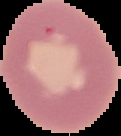
From a thin blood smear. The area outside the segmented cell region is set to black. Result: no malaria parasites detected. Image is 121×136 pixels.